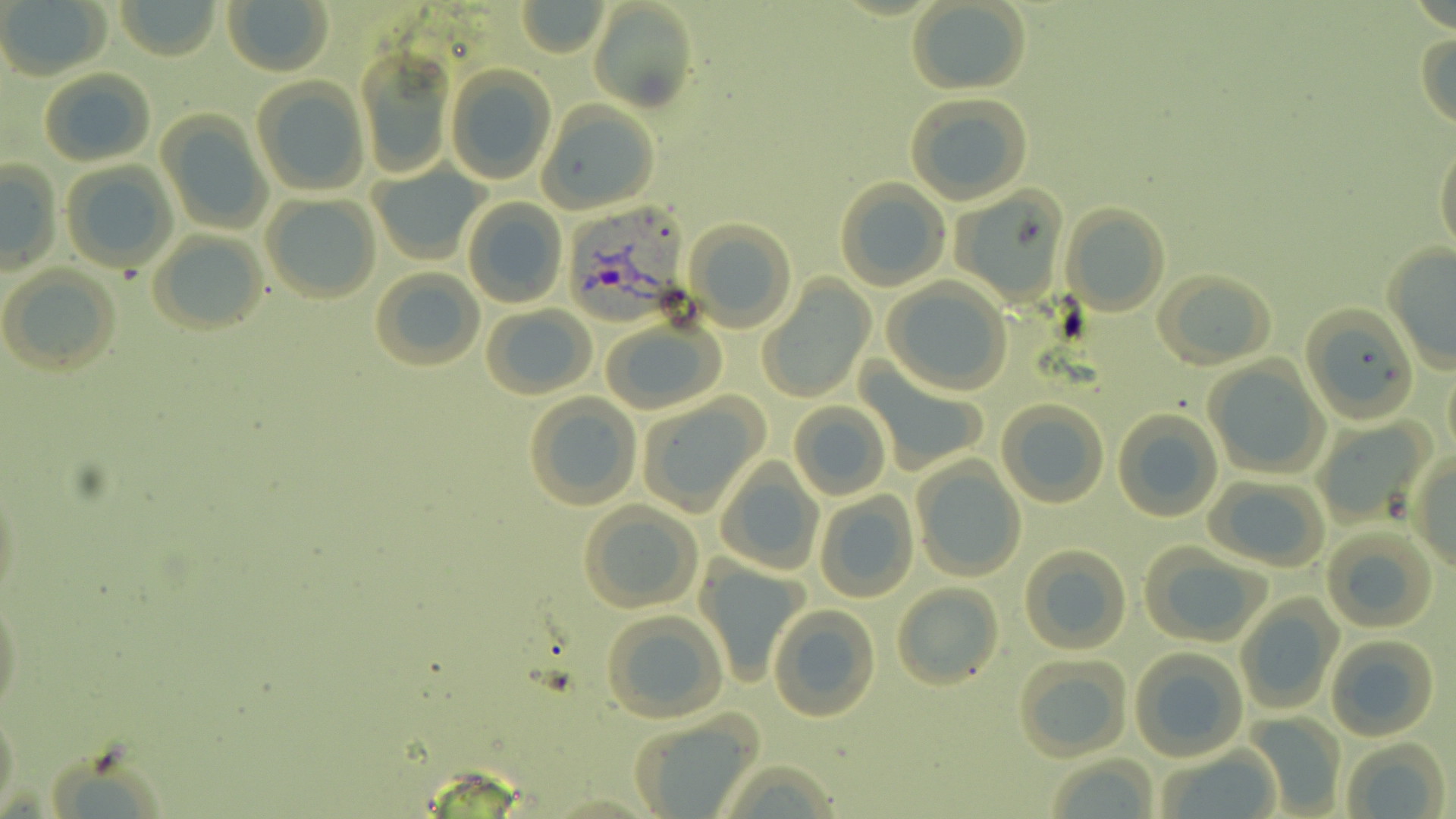
Summary:
  - Coordinate format: approximate bounding boxes as (x1, y1, x2, y2) in pixels
  - Plasmodium vivax-infected red blood cell locations: (565, 203, 689, 336)
  - Uninfected red blood cell locations: (116, 0, 219, 59), (0, 1, 110, 80), (516, 1, 608, 56), (587, 1, 700, 113), (225, 2, 333, 75), (907, 2, 1031, 93), (1416, 29, 1456, 132), (357, 53, 456, 177), (445, 67, 555, 184), (39, 69, 154, 166), (251, 77, 372, 196), (904, 92, 1034, 204), (539, 102, 660, 213), (157, 113, 273, 234), (1434, 140, 1456, 257), (1, 158, 62, 275), (61, 161, 178, 273), (368, 165, 488, 266), (835, 180, 952, 293), (948, 190, 1066, 302), (260, 194, 381, 304), (463, 198, 567, 308), (1061, 204, 1170, 316), (683, 219, 795, 332), (148, 231, 267, 336), (1382, 243, 1456, 375), (0, 264, 121, 378), (369, 268, 484, 372), (1156, 269, 1276, 369), (758, 278, 872, 402), (883, 278, 1014, 396), (480, 304, 596, 400), (1302, 304, 1418, 424), (600, 321, 724, 414), (1203, 360, 1327, 477), (858, 363, 988, 475), (1443, 364, 1456, 456), (637, 394, 770, 515), (523, 395, 642, 512), (996, 399, 1109, 508), (789, 402, 890, 500), (1113, 409, 1223, 522), (1312, 417, 1430, 525), (1410, 453, 1456, 567), (911, 457, 1026, 581), (717, 462, 824, 574), (1, 473, 24, 612), (1205, 475, 1330, 569), (811, 491, 918, 603), (578, 502, 702, 612), (1320, 527, 1437, 634), (1019, 546, 1132, 655), (1141, 547, 1272, 647), (702, 560, 812, 686), (893, 582, 1004, 692), (0, 591, 25, 721), (1236, 597, 1341, 712), (768, 604, 881, 721), (600, 610, 728, 722), (1324, 635, 1438, 742), (1130, 648, 1248, 761), (1013, 655, 1132, 761), (1, 700, 21, 817), (1244, 712, 1346, 814), (627, 713, 766, 816), (1340, 738, 1450, 818), (1157, 748, 1283, 819), (1042, 753, 1160, 818)
  - Slide-level diagnosis: Plasmodium vivax
  - Field of view: one of a larger specimen
  - Image size: 1456×819 pixels
  - Preparation: thin blood film
  - Modality: optical microscopy
  - Stain: May-Grünwald-Giemsa
  - Magnification: 1000x